Report the malaria status of this cell.
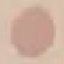
Uninfected.

Acquired by smartphone through the microscope eyepiece. Giemsa stain. Thin smear of blood. Cell patch, automatically extracted from a larger field of view and resized to 64 × 64 pixels.